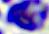

A white blood cell is seen. Captured at 400x magnification. Micrograph.